Mark where leukocytes are.
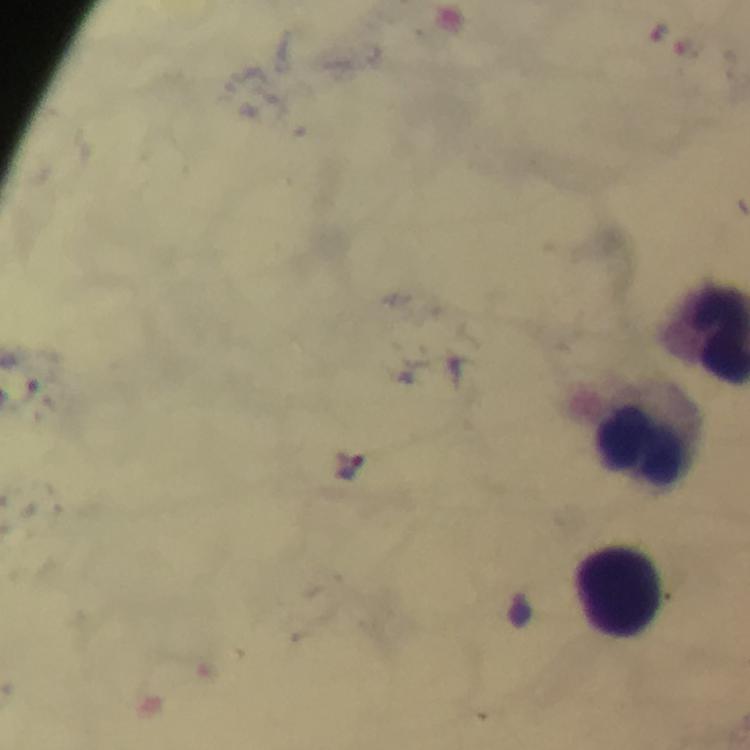
Approximate centers as {x, y} in pixels.
Leukocytes: {639, 444}, {616, 591}.

stain = Giemsa
immersion oil = used
preparation = thick blood smear
context = from a malaria diagnostic workup
capture = smartphone mounted on the microscope
image size = 750×750 pixels
magnification = 100x
malaria parasite locations = approximate centers as {x, y} in pixels: {348, 464}
cropped from = one field of view